Assess the morphology of the red blood cells.
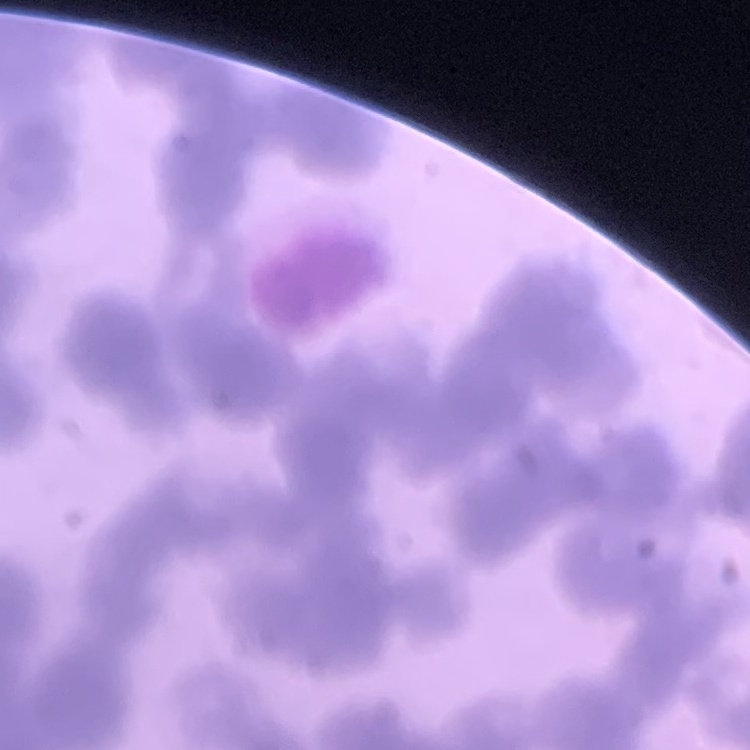
They show rouleaux formation.

Thin peripheral smear. One tile cut from a larger photomicrograph. Field's or Giemsa stain.